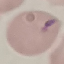
result: malaria parasites identified
image_type: cell patch, automatically extracted from a larger field of view and resized to 64 × 64 pixels
preparation: thin blood film
capture: smartphone through the microscope eyepiece
stain: Giemsa